Comment on the morphology of the erythrocytes.
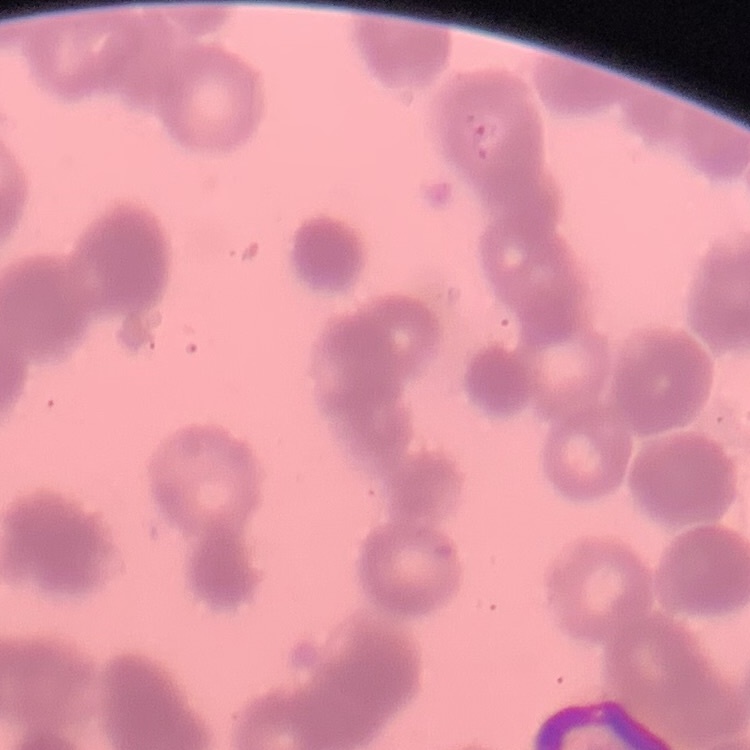

They show rouleaux formation.

preparation = thin blood smear
image type = one tile cut from a larger photomicrograph
stain = Field's or Giemsa